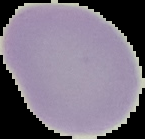
{
  "preparation": "thin blood smear",
  "result": "no Plasmodium parasites seen",
  "image_size": "145×139 pixels",
  "image_type": "cell region segmented out of the field of view; surrounding area masked to black"
}